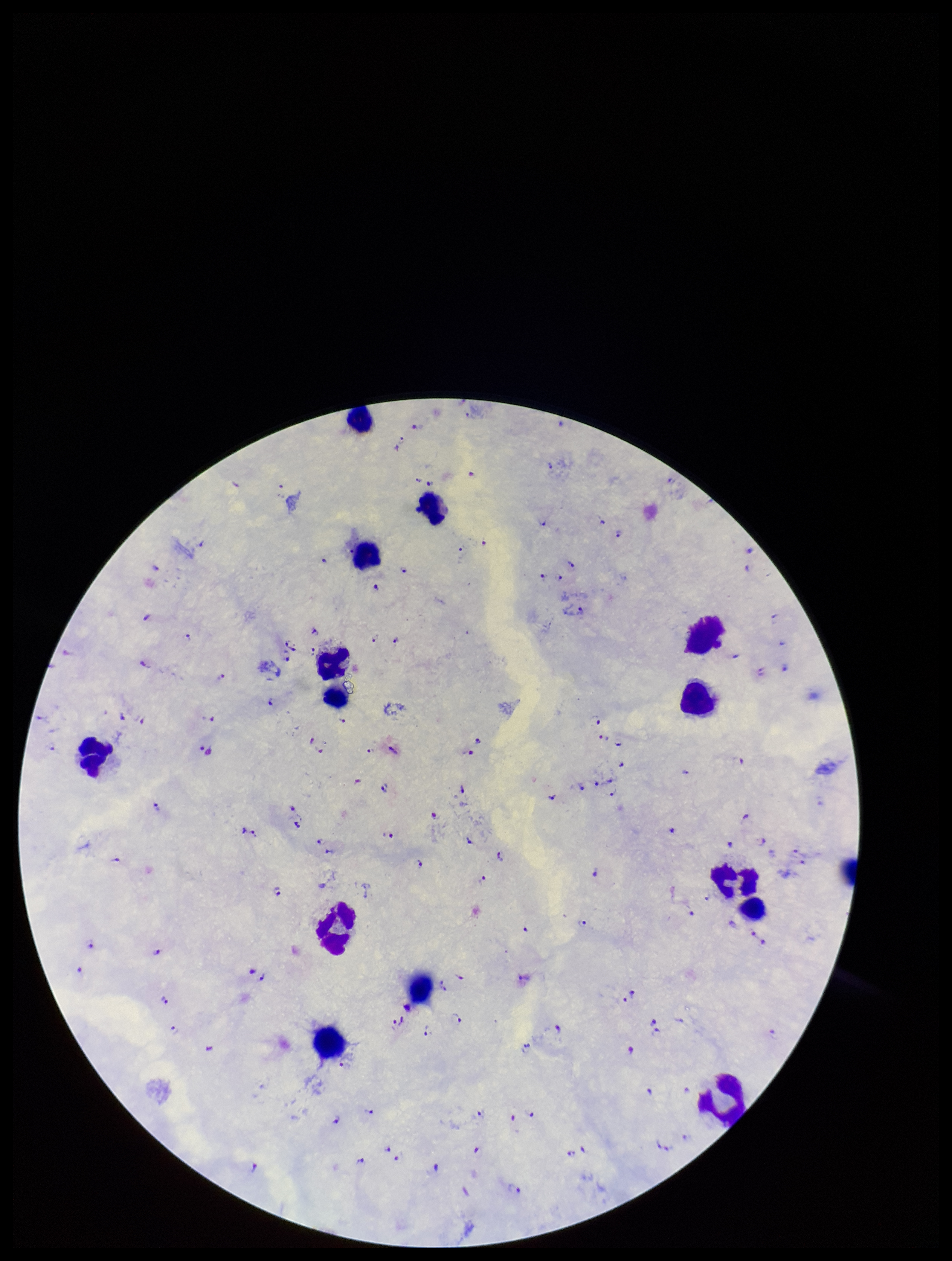
leukocyte count = 14
preparation = thick blood smear
stain = Giemsa
patient malaria status = infected
image size = 952×1261 pixels
species reported for this patient = Plasmodium falciparum
field of view = one from this slide
Plasmodium parasites = detected
parasite count = 153
capture = smartphone photograph through the microscope eyepiece